Comment on the morphology of the red blood cells.
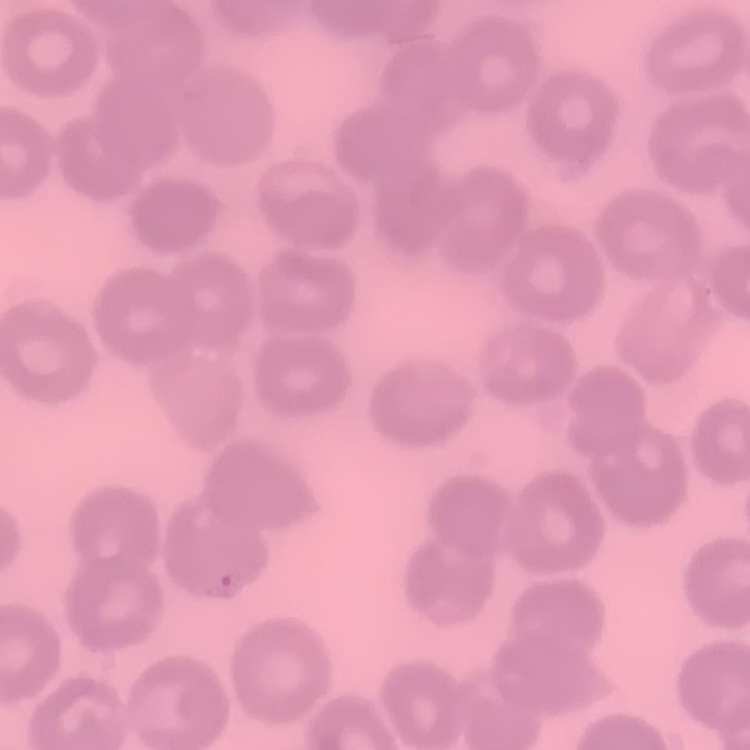

They show no rouleaux formation.

preparation = thin blood smear
stain = Field's or Giemsa
image type = one tile cut from a larger photomicrograph